Report the malaria status of this cell.
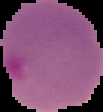
Parasitized.

The area outside the segmented cell region is set to black. From a thin blood film. Image is 103×112 pixels.